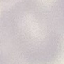

Summary:
  - Result: no malaria parasites detected
  - Preparation: thin blood film
  - Stain: Giemsa
  - Image type: automatically extracted cell patch, resized to 64 × 64 pixels
  - Capture: smartphone camera at the microscope eyepiece